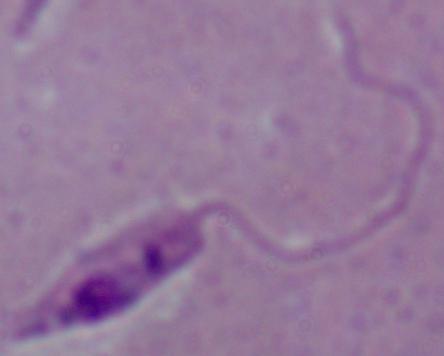

{
  "identification": "Leishmania",
  "magnification": "1000x",
  "modality": "micrograph"
}